Assess this cell for malaria.
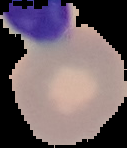
Uninfected.

preparation = thin blood smear
image size = 127×148 pixels
image type = cell region segmented out of the field of view; surrounding area masked to black